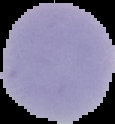
{
  "image_type": "cell region segmented out of the field of view; surrounding area masked to black",
  "result": "no Plasmodium parasites seen",
  "image_size": "115×124 pixels",
  "preparation": "thin blood smear"
}